Report the malaria status of this cell.
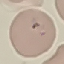
Uninfected.

stain: Giemsa
preparation: thin blood film
capture: smartphone camera at the microscope eyepiece
image_type: automatically extracted cell patch, resized to 64 × 64 pixels